Give the position of every malaria parasite and every leukocyte.
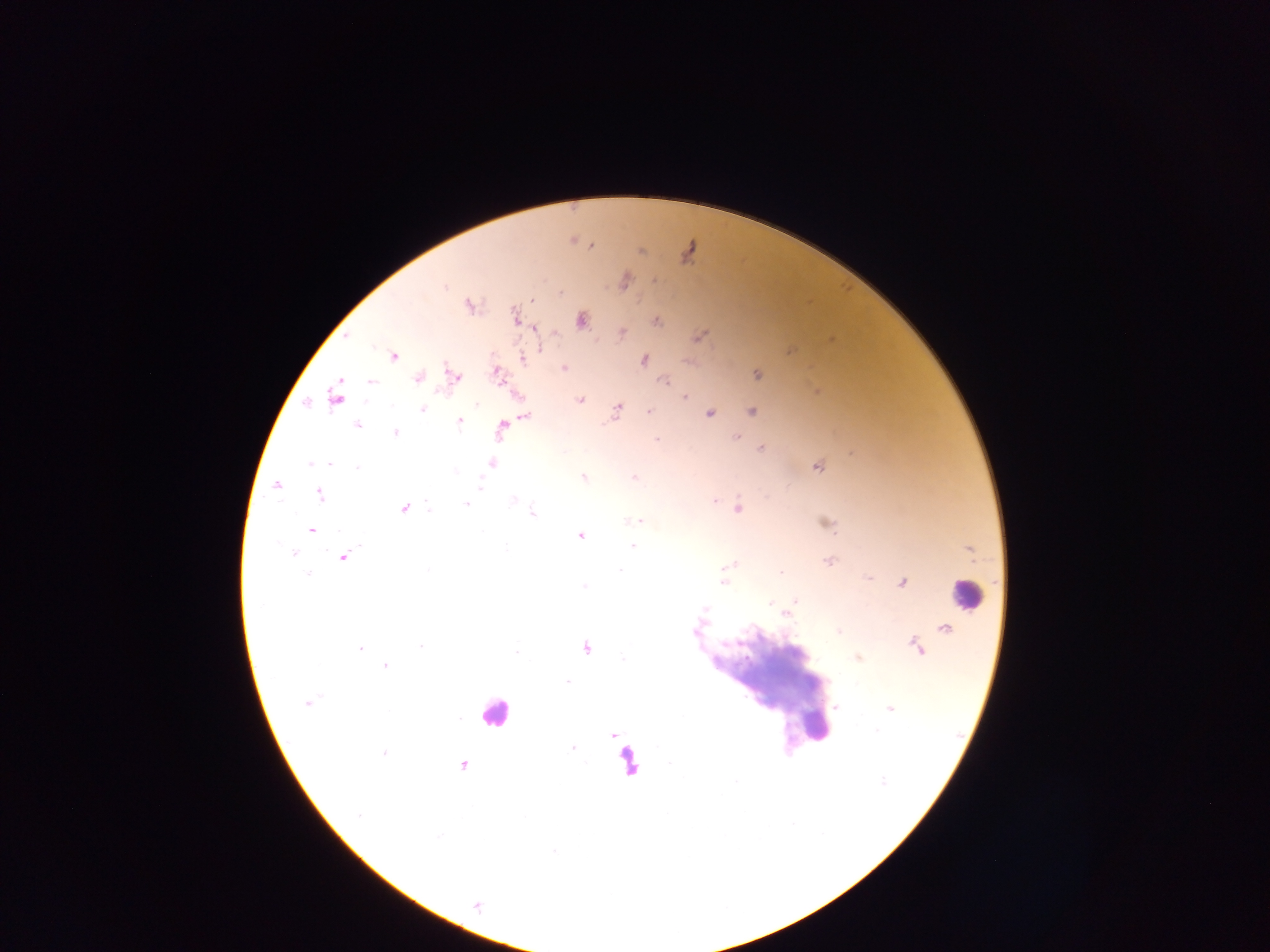
Approximate centers as (x, y) in pixels.
Malaria parasites: (573, 240), (591, 244), (640, 251), (688, 252), (653, 280), (624, 281), (532, 300), (468, 305), (515, 315), (581, 320), (656, 321), (536, 329), (621, 332), (699, 336), (345, 338), (790, 351), (393, 356), (521, 358), (643, 360), (564, 368), (496, 372), (756, 375), (453, 377), (418, 378), (665, 381), (816, 392), (686, 397), (336, 398), (579, 399), (423, 408), (617, 409), (649, 411), (751, 411), (709, 413), (524, 415), (459, 420), (357, 425), (501, 429), (395, 433), (735, 438), (656, 440), (761, 448), (328, 462), (491, 462), (817, 465), (583, 477), (634, 477), (276, 486), (320, 494), (715, 501), (464, 504), (737, 508), (403, 509), (531, 511), (637, 519), (824, 522), (312, 530), (580, 534), (632, 546), (292, 553), (343, 556), (828, 561), (727, 566), (868, 578), (901, 581), (724, 582), (795, 600), (704, 608), (784, 613), (945, 628), (837, 630), (420, 645), (360, 647), (585, 647), (917, 647), (858, 657), (386, 665), (307, 702), (836, 708), (890, 709), (614, 733), (574, 749), (385, 751), (463, 765), (477, 906).
Leukocytes: (967, 595), (495, 712), (815, 727), (629, 762).

Image is 1270×952 pixels. Thick blood smear. Sample from Ghana. Photographed through a microscope with a mobile-phone camera. Single field of view.